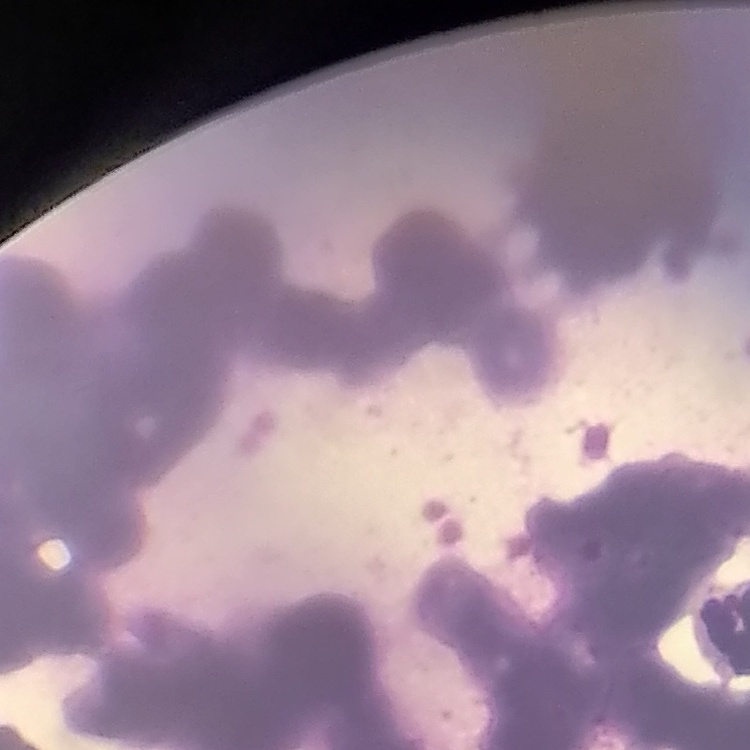

{
  "erythrocyte_morphology": "rouleaux formation",
  "stain": "Field's or Giemsa",
  "image_type": "square crop of a larger photomicrograph",
  "preparation": "thin peripheral smear"
}